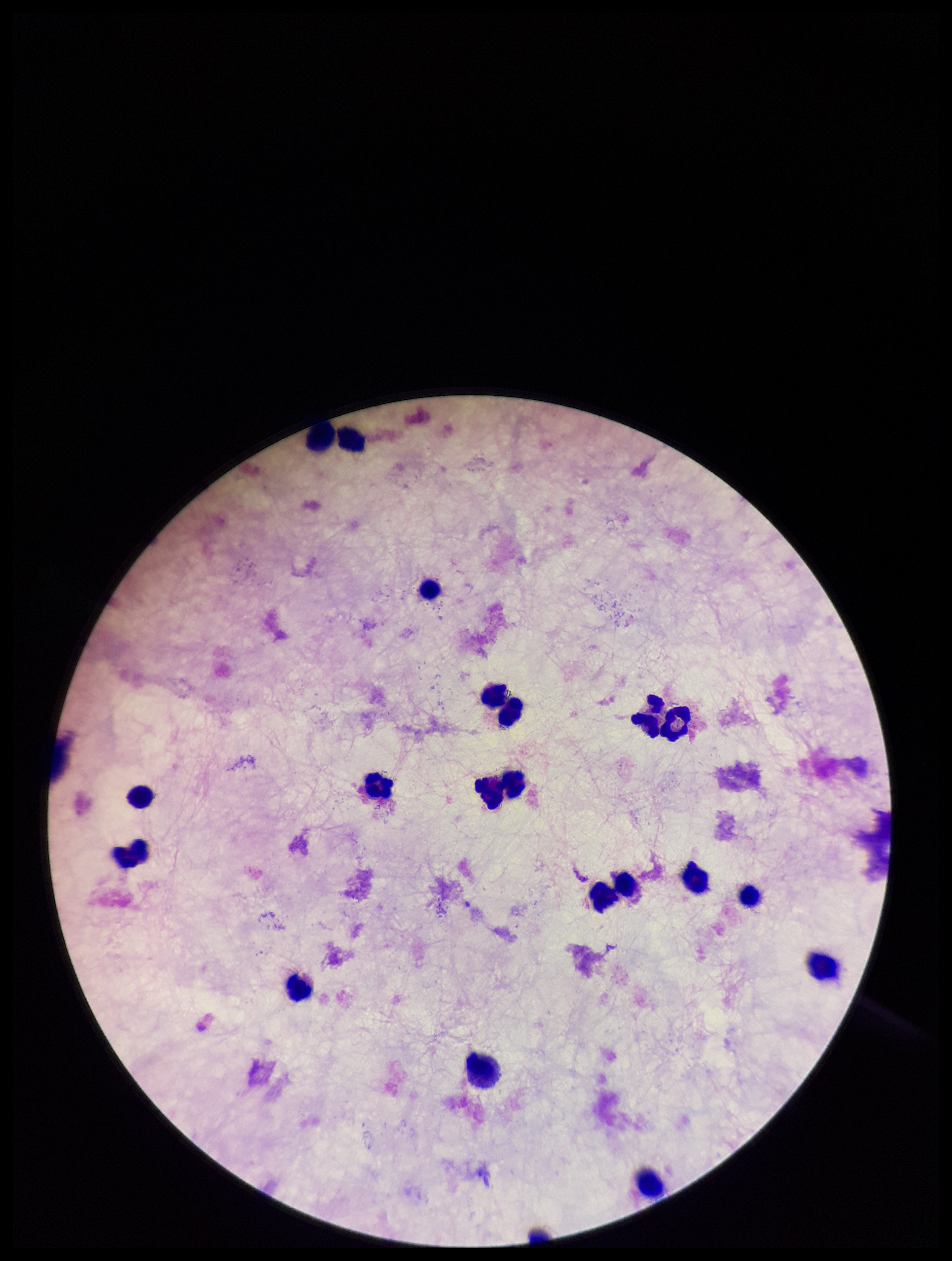 Preparation: thick blood smear. Parasite count: 0. Smartphone photograph taken through the eyepiece of a microscope. Plasmodium parasites: none detected. Patient malaria status: negative. Single field of view. Leukocyte count: 20. Image is 952×1261 pixels. Stained with Giemsa.